Identify the parasite.
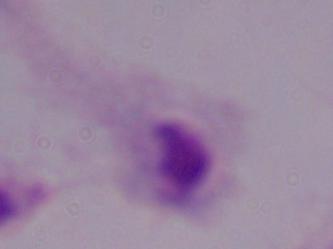

A trichomonad.

magnification = 1000x
modality = photomicrograph